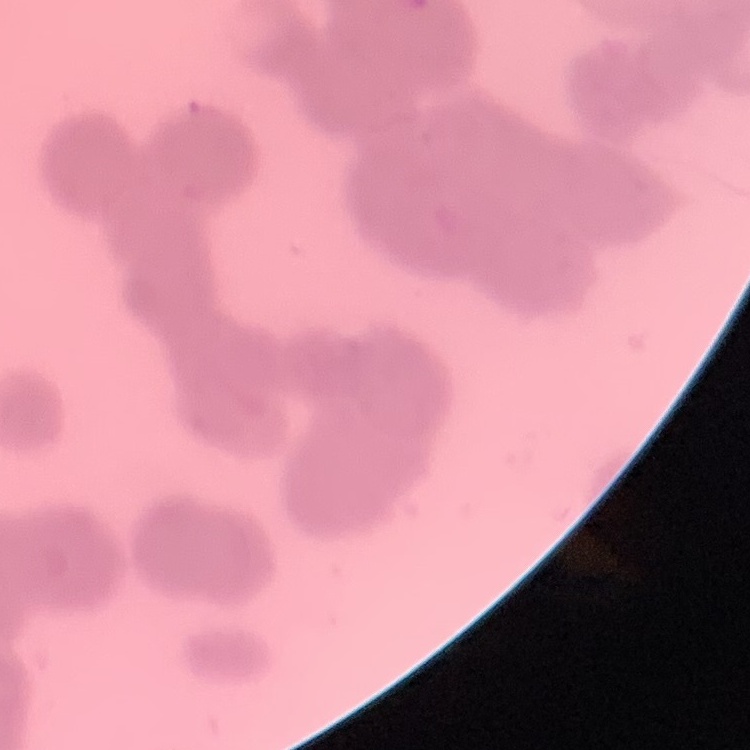 The erythrocytes exhibit rouleaux formation. Thin blood smear. Stained with either Field's or Giemsa. One tile cut from a larger photomicrograph.